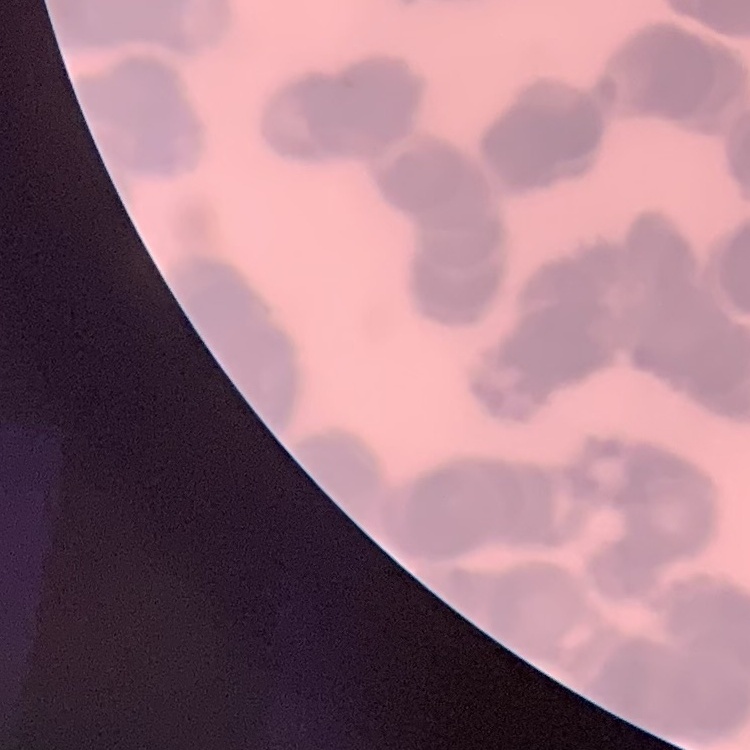

Summary:
  - Red blood cell morphology: rouleaux formation
  - Preparation: thin blood smear
  - Stain: Field's or Giemsa
  - Image type: square crop of a larger photomicrograph